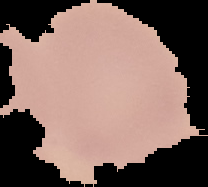

Summary:
  - Preparation: thin blood smear
  - Result: no malaria parasites seen
  - Image type: segmented cell region on a black background
  - Image size: 208×187 pixels